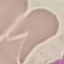 Malaria status: uninfected. Thin blood film. Giemsa-stained preparation. Automatically extracted cell patch, resized to 64 × 64 pixels. Acquired by smartphone through the microscope eyepiece.